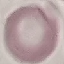

Summary:
  - Result: negative for malaria parasites
  - Preparation: thin smear
  - Stain: Giemsa
  - Capture: smartphone through the microscope eyepiece
  - Image type: cell patch, automatically extracted from a larger field of view and resized to 64 × 64 pixels